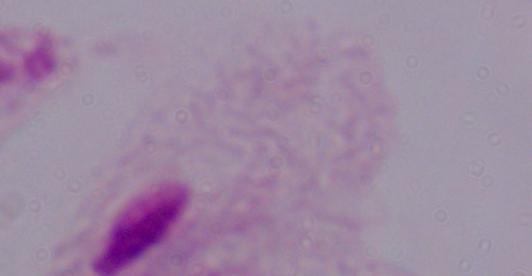

A trichomonad is seen. Photomicrograph. Captured at 1000x magnification.